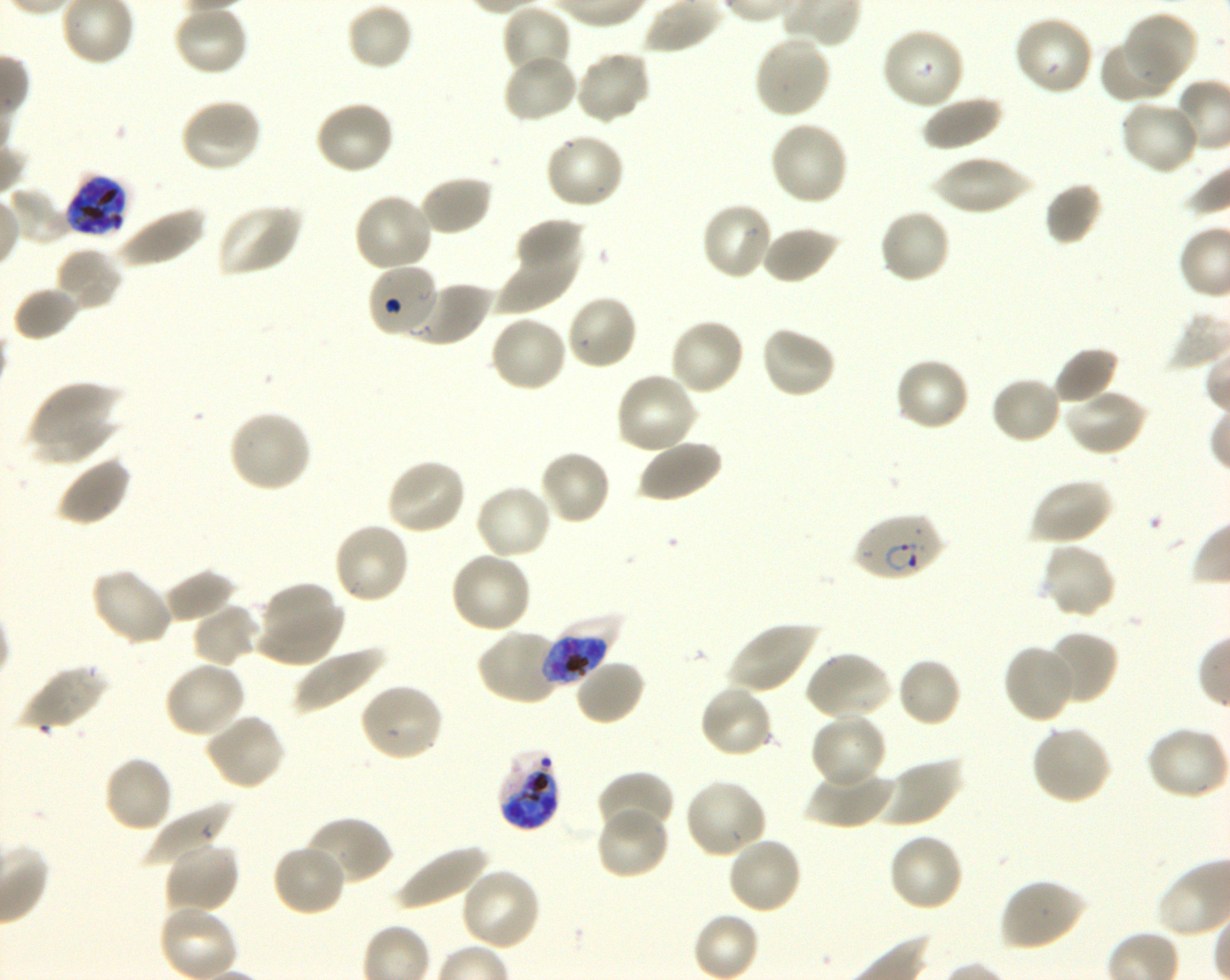

Approximate bounding boxes as (x1, y1, x2, y2) in pixels. Not every red blood cell is marked. A life-cycle stage — or a range of stages, where the recorded stages span more than one — follows each staged infected red blood cell.
Summary:
  - Locations of red blood cells of indeterminate infection status: (366, 263, 438, 338)
  - Locations of uninfected red blood cells: (346, 2, 414, 71), (172, 4, 249, 78), (501, 4, 572, 80), (1123, 10, 1198, 87), (1012, 14, 1095, 97), (880, 26, 966, 112), (753, 34, 832, 119), (1099, 38, 1178, 103), (502, 51, 579, 124), (574, 51, 650, 125), (921, 94, 1003, 151), (178, 97, 262, 174), (1118, 97, 1201, 177), (313, 100, 396, 177), (768, 119, 849, 207), (543, 132, 626, 211), (930, 155, 1035, 215), (418, 174, 493, 236), (1045, 182, 1103, 246), (6, 187, 72, 245), (353, 191, 434, 273), (700, 201, 775, 280), (215, 202, 302, 277), (115, 204, 206, 269), (877, 208, 952, 285), (514, 217, 584, 275), (760, 224, 842, 284), (496, 225, 582, 314), (54, 246, 124, 312), (402, 279, 490, 347), (12, 285, 81, 341), (565, 295, 640, 372), (488, 314, 569, 393), (668, 317, 746, 397), (759, 326, 837, 400), (1053, 346, 1119, 408), (894, 356, 971, 432), (615, 371, 699, 456), (990, 375, 1062, 445), (27, 380, 123, 465), (27, 380, 123, 441), (1063, 388, 1148, 457), (227, 409, 313, 494), (29, 416, 123, 465), (637, 438, 722, 503), (538, 448, 612, 526), (55, 454, 132, 528), (385, 457, 468, 536), (1028, 477, 1114, 546), (474, 484, 553, 562), (331, 521, 411, 605), (1039, 542, 1117, 620), (449, 550, 533, 634), (89, 566, 173, 646), (164, 570, 238, 625), (255, 581, 345, 667), (191, 603, 261, 667), (726, 620, 820, 694), (477, 629, 563, 706), (1046, 629, 1119, 705), (1001, 642, 1078, 725), (293, 645, 385, 715), (805, 650, 893, 722), (896, 656, 962, 727), (574, 658, 646, 726), (164, 661, 245, 739), (17, 663, 107, 733), (358, 681, 445, 763), (699, 684, 774, 759), (203, 712, 286, 791), (809, 712, 886, 790), (1030, 723, 1113, 806), (1145, 726, 1229, 801), (102, 755, 174, 833), (876, 757, 962, 829), (805, 765, 893, 828), (596, 771, 674, 836), (682, 777, 768, 859), (144, 802, 234, 872), (595, 805, 670, 880), (303, 815, 394, 887), (887, 832, 965, 912), (725, 835, 804, 916), (164, 840, 240, 916), (394, 842, 490, 912), (272, 843, 348, 918), (460, 866, 542, 951), (999, 877, 1087, 952), (158, 905, 238, 980), (693, 911, 759, 980)
  - Locations of infected red blood cells: (63, 172, 131, 239) late trophozoite to late schizont; (852, 511, 944, 582) ring; (543, 618, 616, 686) late trophozoite to late schizont; (496, 750, 562, 832) late trophozoite to late schizont
  - Culture: shaking in-vitro Plasmodium falciparum strain 3D7
  - Field of view: single
  - Donor blood group: O+
  - Preparation: thin blood film
  - Image size: 1230×980 pixels
  - Objective: 100x, oil immersion, numerical aperture 1.30
  - Stain: Giemsa